Assess this cell for malaria.
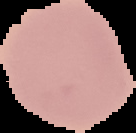

Uninfected.

Cell region segmented out of the field of view; the surrounding area is masked to black. From a thin blood smear. Image is 136×133 pixels.